Describe the morphology of the red blood cells.
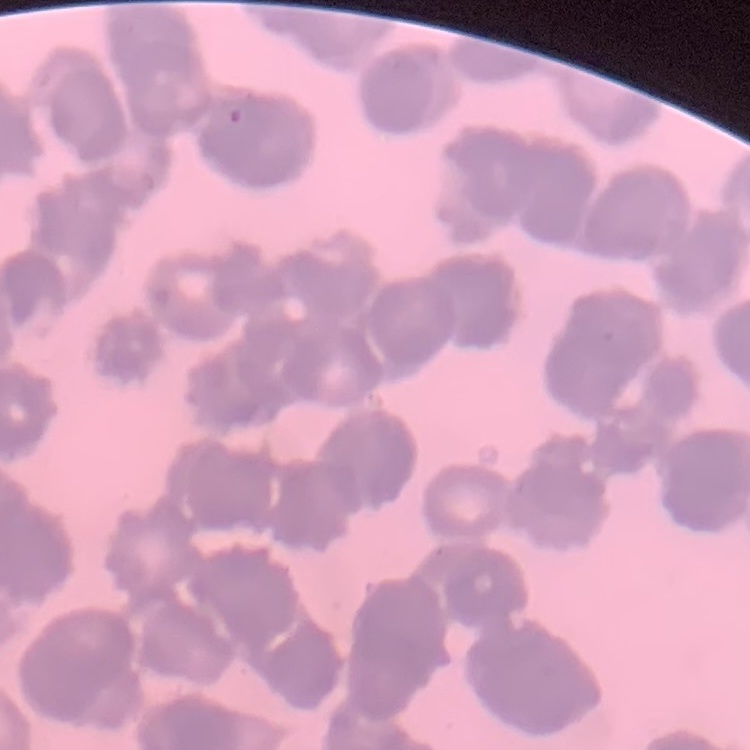
They show rouleaux formation.

Square crop of a larger photomicrograph. Thin peripheral smear. Field's or Giemsa stain.